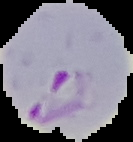

{
  "image_type": "cell region segmented out of the field of view; surrounding area masked to black",
  "preparation": "thin blood film",
  "result": "malaria parasites identified",
  "image_size": "133×142 pixels"
}